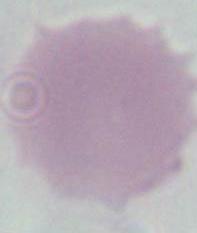

Micrograph. An erythrocyte is seen. 1000x magnification.